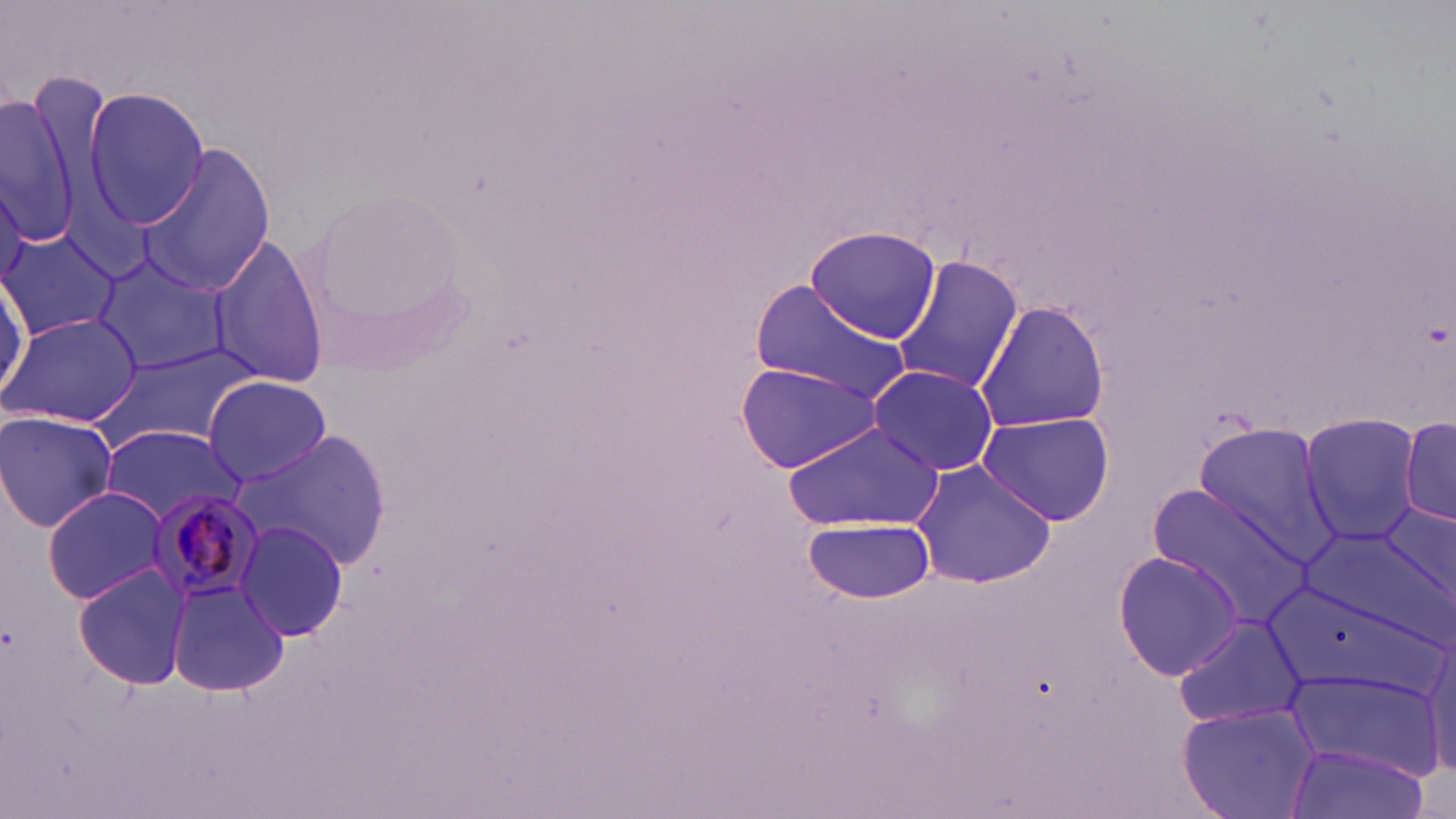
Approximate bounding boxes as (x1,y1)-(x2,y2) corner pairs in pixels. Plasmodium malariae-infected red blood cell locations: (142,488)-(265,606). Uninfected red blood cell locations: (0,86)-(84,252), (84,87)-(209,230), (138,142)-(278,295), (0,183)-(27,292), (0,225)-(119,342), (806,226)-(941,344), (205,233)-(330,392), (91,251)-(231,378), (890,256)-(1024,396), (0,270)-(28,407), (748,280)-(910,403), (974,301)-(1111,433), (3,312)-(141,428), (94,342)-(259,450), (733,359)-(884,473), (868,364)-(999,476), (203,375)-(332,486), (0,410)-(119,531), (978,410)-(1116,528), (1299,413)-(1424,543), (1399,414)-(1456,529), (783,421)-(943,530), (100,423)-(242,526), (1190,424)-(1338,560), (237,429)-(392,569), (910,458)-(1058,591), (41,487)-(174,605), (1147,488)-(1311,626), (1375,501)-(1456,616), (804,516)-(937,604), (235,520)-(352,642), (1298,523)-(1452,641), (1111,551)-(1246,680), (74,565)-(190,688), (168,578)-(288,696), (1173,614)-(1309,730), (1421,632)-(1456,778), (1286,665)-(1444,783), (1182,706)-(1317,818), (1289,742)-(1431,819). Slide-level diagnosis: Plasmodium malariae. Image is 1456×819 pixels. May-Grünwald-Giemsa-stained preparation. Thin blood smear. Light microscopy. Captured at 1000x magnification. One field of a larger specimen.